State the blood parasite species.
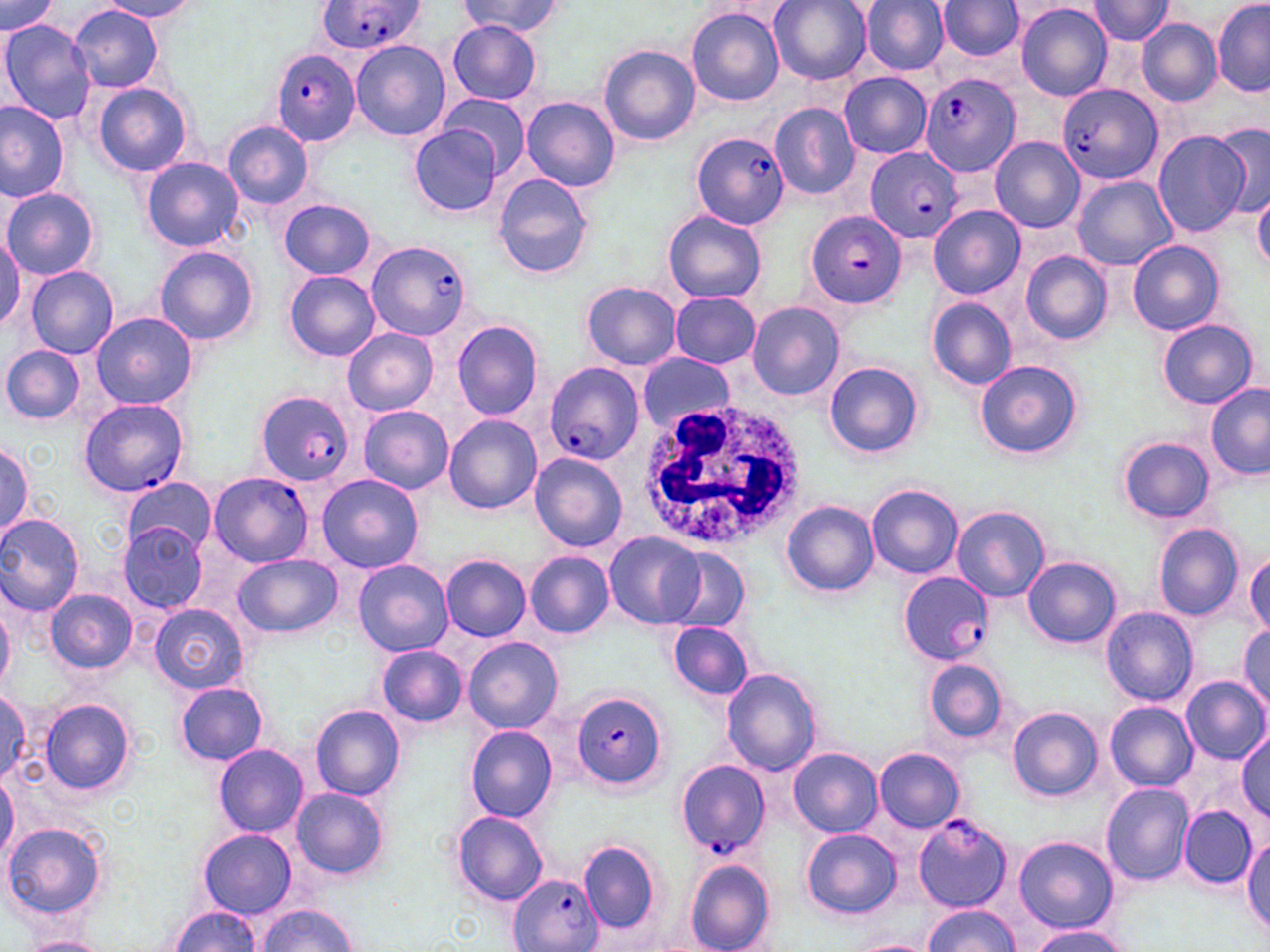
Plasmodium falciparum.

field of view = single
preparation = thin blood film
uninfected red blood cell locations = approximate bounding boxes as (x1,y1)-(x2,y2) corner pairs in pixels: (460,0)-(566,36), (769,0)-(872,85), (860,0)-(950,75), (1087,0)-(1176,44), (0,1)-(61,36), (98,1)-(202,22), (1212,1)-(1269,98), (935,2)-(1023,60), (1015,2)-(1113,102), (70,5)-(164,94), (687,8)-(786,107), (1136,18)-(1222,105), (0,20)-(97,126), (446,22)-(543,105), (351,41)-(450,141), (598,45)-(701,147), (840,72)-(932,158), (91,82)-(194,177), (439,92)-(532,176), (521,96)-(620,192), (0,101)-(70,202), (769,103)-(860,200), (222,119)-(314,209), (1210,121)-(1270,223), (409,126)-(501,216), (1152,130)-(1250,238), (989,137)-(1085,233), (141,156)-(244,251), (492,172)-(596,280), (1072,175)-(1176,270), (3,187)-(99,280), (1252,189)-(1270,275), (277,198)-(377,280), (928,206)-(1024,300), (662,209)-(767,305), (0,229)-(25,332), (1126,238)-(1225,335), (156,245)-(259,346), (1021,251)-(1114,343), (24,265)-(119,358), (284,271)-(381,360), (582,281)-(682,371), (669,293)-(761,368), (927,298)-(1016,389), (747,301)-(846,401), (91,310)-(197,409), (1157,318)-(1259,409), (450,320)-(544,420), (342,327)-(438,417), (1,344)-(86,424), (637,353)-(736,432), (974,358)-(1083,459), (824,362)-(925,457), (1205,383)-(1270,481), (358,405)-(454,494), (443,414)-(543,515), (1117,436)-(1215,524), (0,442)-(32,540), (529,453)-(627,552), (317,474)-(424,574), (122,478)-(218,557), (866,482)-(963,579), (782,501)-(879,596), (952,505)-(1049,602), (0,512)-(85,616), (118,523)-(210,614), (1154,523)-(1244,622), (603,532)-(705,629), (661,547)-(749,633), (525,550)-(613,639), (1245,551)-(1270,637), (232,553)-(343,638), (440,554)-(531,641), (1023,556)-(1120,647), (353,559)-(452,657), (45,589)-(136,674), (0,601)-(15,692), (150,603)-(248,695), (162,606)-(261,766), (1101,606)-(1198,706), (667,621)-(754,700), (1238,626)-(1270,714), (463,636)-(564,735), (376,644)-(469,728), (925,658)-(1009,744), (722,667)-(822,775), (1179,676)-(1269,764), (175,681)-(268,765), (0,691)-(32,788), (40,697)-(136,797), (1105,701)-(1198,791), (310,704)-(405,801), (1007,707)-(1102,802), (466,725)-(558,821), (1235,730)-(1270,818), (212,744)-(308,836), (788,747)-(882,837), (874,748)-(966,832), (0,772)-(19,865), (1101,783)-(1195,885), (290,786)-(390,881), (1179,806)-(1256,889), (452,810)-(548,906), (4,821)-(107,921), (802,828)-(902,919), (199,829)-(297,917), (1243,831)-(1269,936), (1013,836)-(1117,932), (579,841)-(661,937), (683,859)-(778,952), (255,903)-(359,952), (922,905)-(1020,951), (169,906)-(261,952), (1023,923)-(1134,952), (24,935)-(107,951), (849,938)-(939,952)
image size = 1270×952 pixels
stain = May-Grünwald-Giemsa
Plasmodium falciparum-infected red blood cell locations = approximate bounding boxes as (x1,y1)-(x2,y2) corner pairs in pixels: (317,1)-(425,54), (271,48)-(360,145), (920,72)-(1019,178), (1057,83)-(1162,184), (690,132)-(789,228), (864,145)-(963,243), (804,212)-(906,309), (366,241)-(472,340), (544,362)-(644,464), (253,390)-(355,484), (78,397)-(189,498), (208,473)-(313,566), (898,570)-(992,666), (574,691)-(670,789), (676,759)-(770,856), (913,813)-(1011,913), (506,872)-(605,952)
white blood cell locations = approximate bounding boxes as (x1,y1)-(x2,y2) corner pairs in pixels: (633,393)-(809,551)
modality = optical microscopy
magnification = 1000x